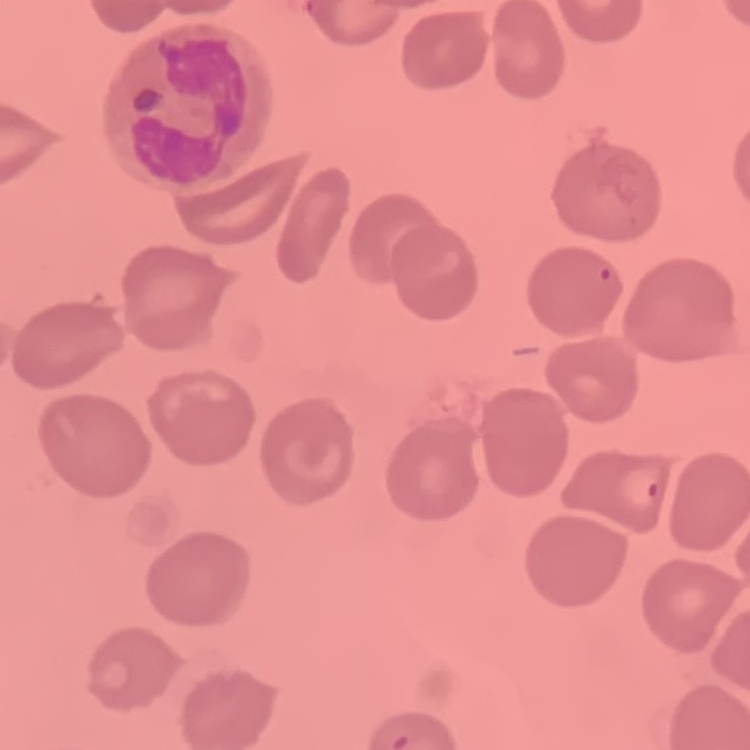

Summary:
  - Erythrocyte morphology: no rouleaux formation
  - Stain: Field's or Giemsa
  - Image type: square crop of a larger photomicrograph
  - Preparation: thin blood smear